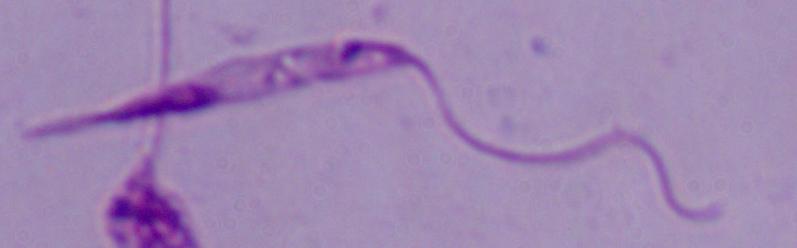

{
  "modality": "photomicrograph",
  "magnification": "1000x",
  "identification": "Leishmania"
}